Locate every blood parasite and identify its species.
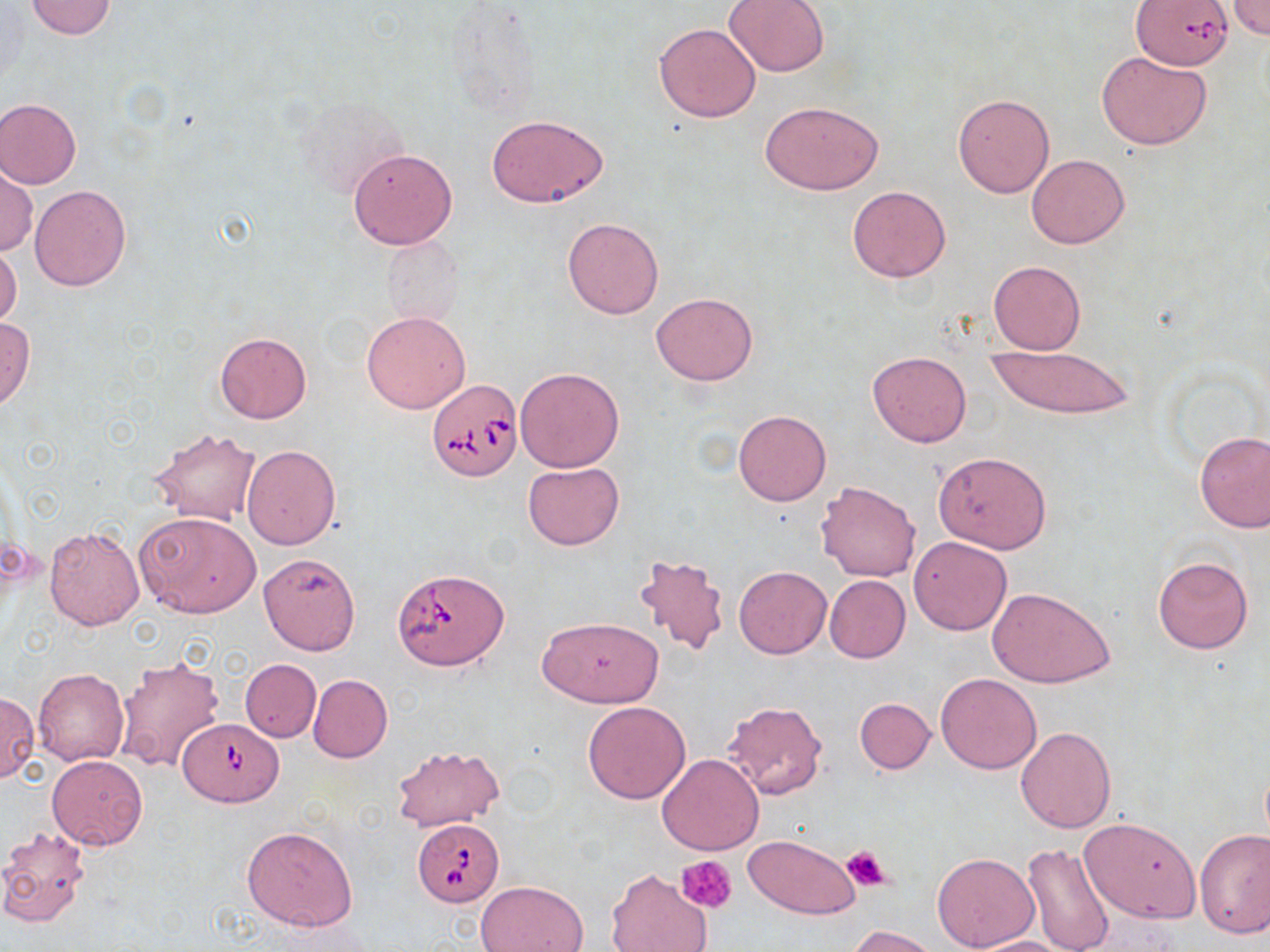

Approximate bounding boxes as (x1,y1)-(x2,y2) corner pairs in pixels.
Babesia divergens-infected red blood cells: (1131,0)-(1235,71), (427,379)-(523,482), (393,567)-(509,672), (180,717)-(280,807), (412,817)-(504,907).
No Plasmodium falciparum, Plasmodium ovale, Plasmodium malariae, Plasmodium vivax, or Trypanosoma brucei observed.

Uninfected red blood cell locations: (24,0)-(117,40), (724,0)-(830,77), (1227,0)-(1270,40), (442,3)-(543,121), (653,22)-(761,122), (1097,49)-(1211,151), (953,93)-(1055,198), (0,97)-(81,189), (759,99)-(885,195), (307,103)-(408,201), (486,115)-(610,209), (347,147)-(458,250), (1026,154)-(1130,249), (1,165)-(37,255), (29,184)-(132,291), (846,186)-(951,282), (562,218)-(664,319), (381,237)-(464,328), (0,240)-(21,331), (988,260)-(1084,354), (651,292)-(758,385), (360,310)-(471,414), (0,316)-(35,409), (215,332)-(312,423), (987,346)-(1135,417), (867,351)-(971,447), (514,367)-(625,472), (733,410)-(830,505), (149,427)-(262,524), (1194,431)-(1270,533), (242,444)-(341,550), (933,451)-(1051,553), (523,462)-(624,549), (815,481)-(920,582), (136,511)-(261,619), (43,525)-(144,630), (908,536)-(1012,635), (259,552)-(361,654), (634,554)-(729,655), (1152,555)-(1254,654), (734,566)-(832,660), (825,575)-(911,663), (989,586)-(1116,689), (537,616)-(664,707), (114,655)-(225,776), (241,659)-(321,742), (33,668)-(129,766), (935,673)-(1042,774), (308,675)-(392,763), (0,692)-(39,783), (855,697)-(935,773), (720,701)-(827,800), (582,702)-(691,803), (1016,726)-(1116,833), (391,745)-(505,832), (656,754)-(764,855), (46,755)-(149,850), (1078,817)-(1200,923), (1,825)-(93,928), (241,825)-(358,931), (1195,828)-(1270,939), (743,835)-(861,919), (1022,843)-(1115,952), (931,852)-(1040,951), (605,868)-(714,952), (477,880)-(588,952), (846,925)-(940,951), (966,936)-(1080,952). Platelet locations: (841,843)-(892,891), (677,856)-(738,914). Slide-level diagnosis: Babesia divergens. May-Grünwald-Giemsa-stained preparation. Image is 1270×952 pixels. Captured at 1000x magnification. Single field of view. Thin blood smear. Optical microscopy.